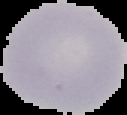
preparation = thin blood smear
image type = segmented cell region with the area outside set to black
result = negative for Plasmodium parasites
image size = 127×115 pixels